Report the malaria status of this cell.
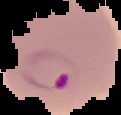

Parasitized.

Summary:
  - Preparation: thin blood smear
  - Image type: segmented cell region on a black background
  - Image size: 121×115 pixels